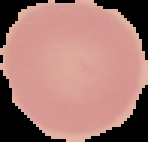

Summary:
  - Preparation: thin blood film
  - Image type: cell region segmented out of the field of view; surrounding area masked to black
  - Image size: 148×142 pixels
  - Malaria status: uninfected